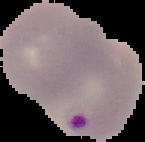
image type = segmented cell region on a black background
image size = 145×142 pixels
result = Plasmodium parasites identified
preparation = thin blood smear